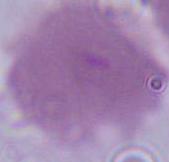

Summary:
  - Modality: micrograph
  - Identification: red blood cell
  - Magnification: 1000x